Classify this cell by malaria status.
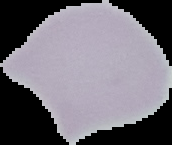

It is uninfected.

Summary:
  - Image type: segmented cell region with the area outside set to black
  - Preparation: thin blood smear
  - Image size: 172×145 pixels